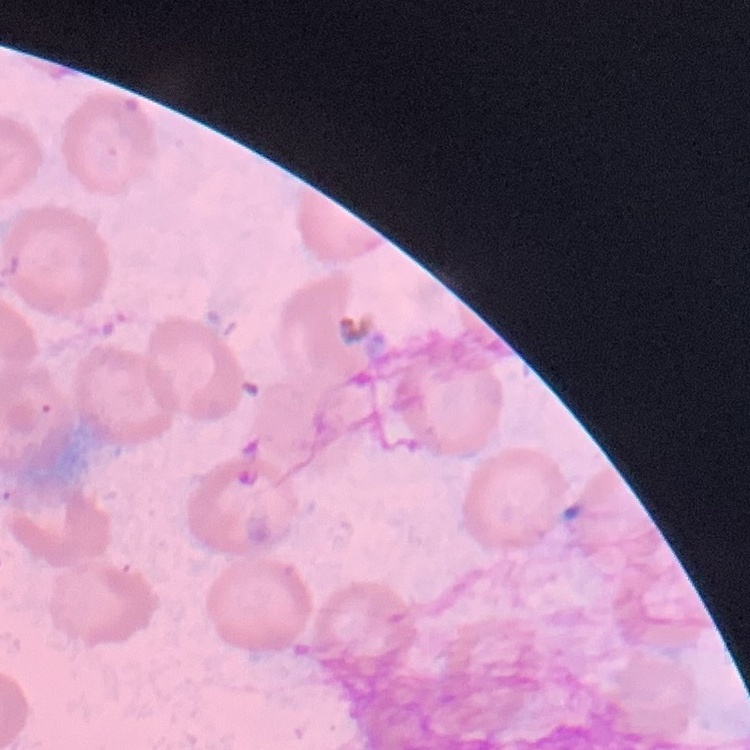

The red blood cells exhibit no rouleaux formation. Field's or Giemsa stain. Thin peripheral smear. One tile cut from a larger photomicrograph.